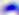

400x magnification. Toxoplasma gondii is seen. Photomicrograph.